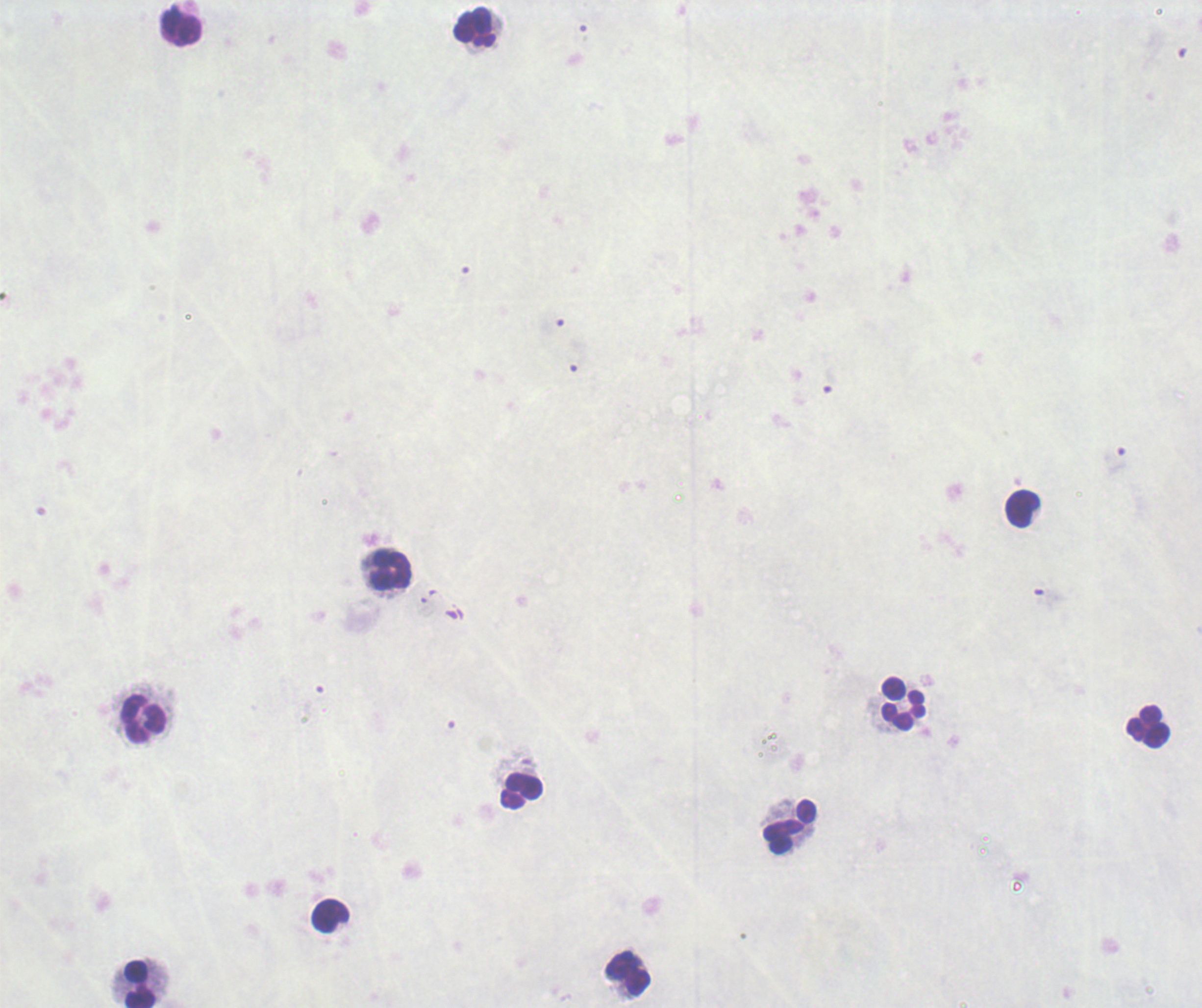
Approximate centers as [x, y] in pixels.
Summary:
  - Leukocyte locations: [476, 27], [182, 28], [1022, 509], [391, 572], [903, 703], [144, 719], [1148, 727], [521, 791], [790, 826], [331, 916], [628, 974], [140, 985]
  - Magnification: 100x
  - Field of view: one from this slide
  - Image size: 1202×1008 pixels
  - Stain: Romanowsky
  - Result: no Plasmodium parasites detected
  - Background quality: poor
  - Context: previously used in a real diagnosis
  - Preparation: thick blood smear